Give the position of every Plasmodium parasite visible.
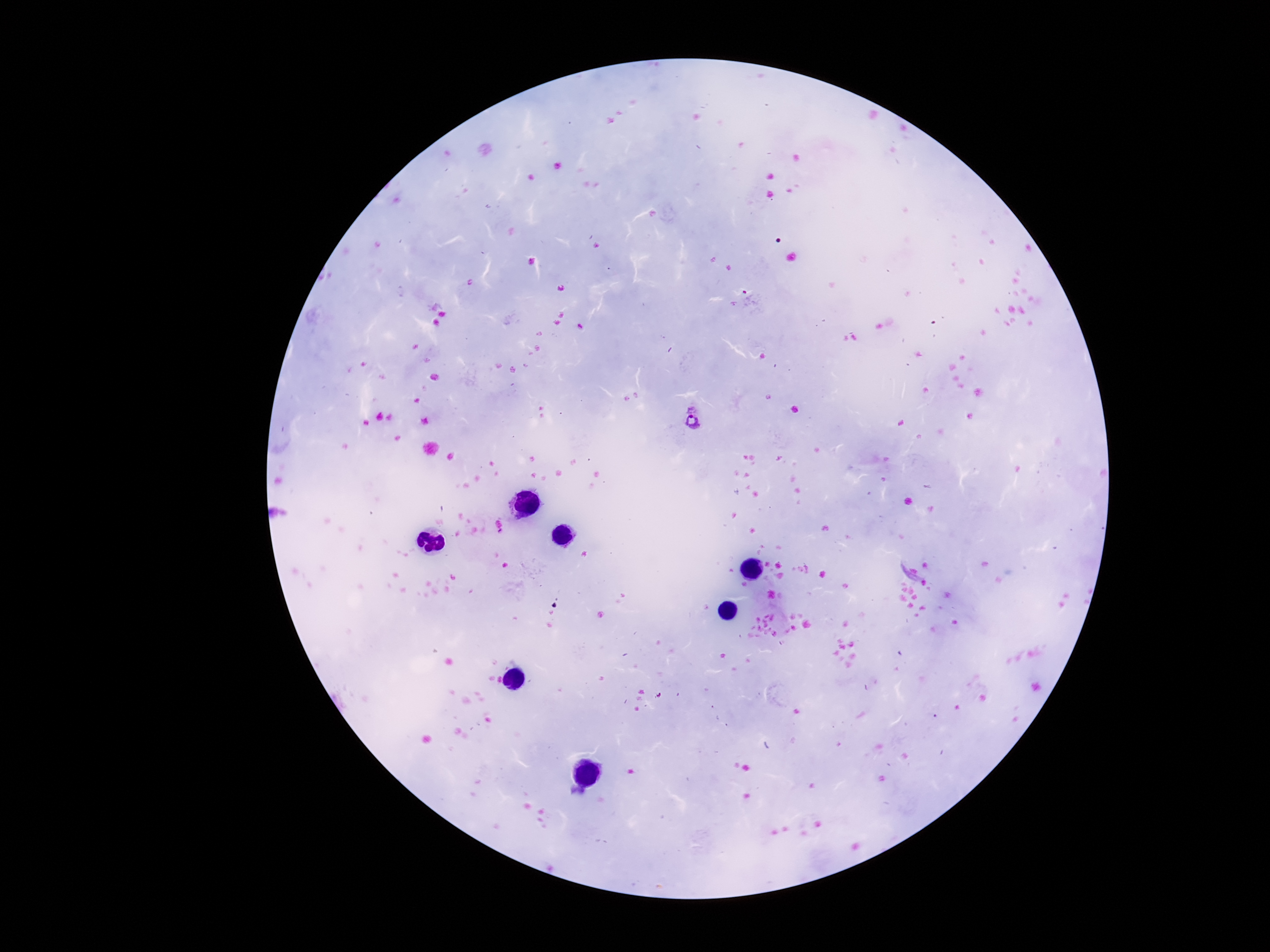

Approximate centers as [x, y] in pixels.
Plasmodium parasites: [691, 418].

100x magnification. Patient malaria status: positive. One field from this slide. Image is 1270×952 pixels. Giemsa-stained preparation. Photographed through the microscope eyepiece with a smartphone camera. Thick blood film.